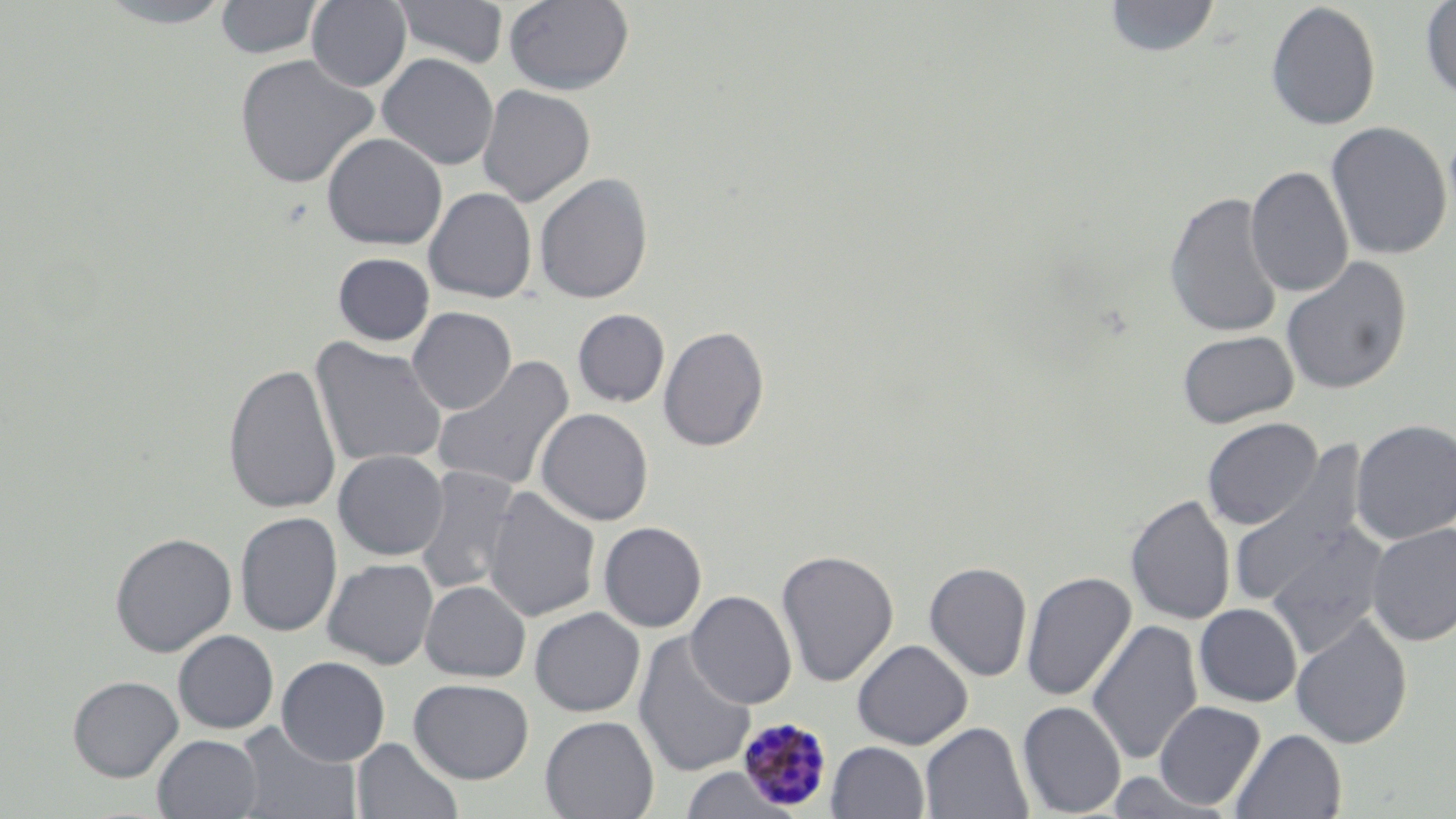

plasmodium_malariae_infected_red_blood_cell_locations: 'approximate bounding boxes as (x1,y1)-(x2,y2) corner pairs in pixels: (737,716)-(834,811)'
slide_level_diagnosis: Plasmodium malariae
modality: optical microscopy
field_of_view: one of a larger specimen
magnification: 1000x
stain: May-Grünwald-Giemsa
image_size: 1456×819 pixels
preparation: thin blood film
uninfected_red_blood_cell_locations: 'approximate bounding boxes as (x1,y1)-(x2,y2) corner pairs in pixels: (92,0)-(239,28), (215,0)-(324,60), (306,0)-(412,92), (392,0)-(509,69), (504,0)-(634,95), (1103,0)-(1220,58), (1420,1)-(1456,102), (1266,2)-(1382,131), (234,53)-(379,190), (376,53)-(499,171), (477,85)-(596,207), (1326,121)-(1452,260), (322,132)-(447,250), (1245,165)-(1354,298), (534,173)-(654,304), (424,187)-(537,304), (1164,191)-(1284,339), (332,252)-(434,346), (1280,256)-(1413,395), (407,307)-(516,414), (573,309)-(670,407), (659,324)-(770,452), (1177,330)-(1298,428), (311,338)-(448,470), (431,355)-(575,494), (223,362)-(342,515), (535,408)-(654,526), (1201,417)-(1323,530), (1351,419)-(1456,544), (333,449)-(449,560), (1226,458)-(1375,615), (414,466)-(522,597), (483,486)-(601,623), (1126,494)-(1235,625), (235,512)-(342,636), (598,522)-(707,632), (1264,522)-(1388,658), (1366,523)-(1456,645), (110,532)-(237,657), (776,548)-(899,687), (322,558)-(438,669), (924,561)-(1033,682), (1021,570)-(1137,701), (420,580)-(531,682), (686,590)-(797,709), (1194,603)-(1302,707), (529,607)-(645,717), (1291,615)-(1413,749), (1087,620)-(1203,765), (172,630)-(279,733), (633,633)-(757,778), (852,639)-(973,750), (276,656)-(390,766), (67,675)-(183,781), (408,678)-(534,784), (1154,700)-(1266,810), (1017,701)-(1126,817), (540,715)-(659,819), (921,722)-(1032,818), (233,723)-(362,819), (1231,728)-(1347,818), (153,734)-(262,818), (352,737)-(463,819), (827,741)-(929,819), (678,768)-(798,819)'